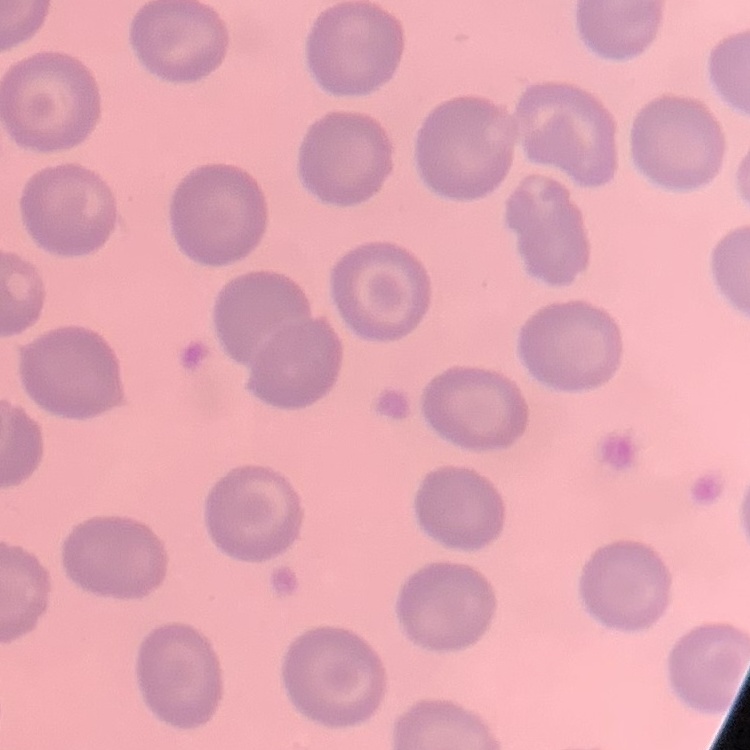
red blood cell morphology = no rouleaux formation
image type = square crop of a larger photomicrograph
stain = Field's or Giemsa
preparation = thin blood film